Comment on the morphology of the erythrocytes.
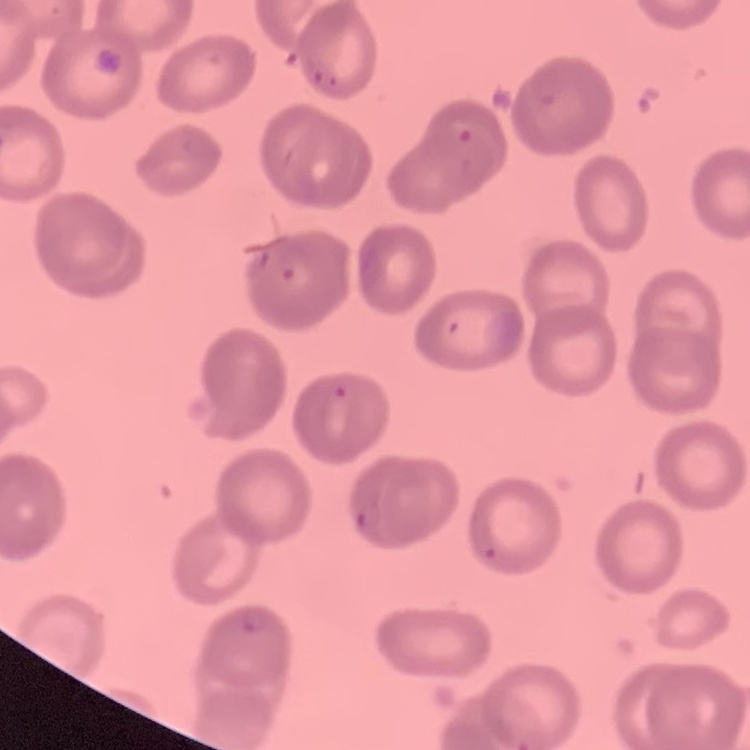
They show no rouleaux formation.

Thin blood film. Square crop of a larger photomicrograph. Stained with either Field's or Giemsa.